Locate every uninfected red blood cell.
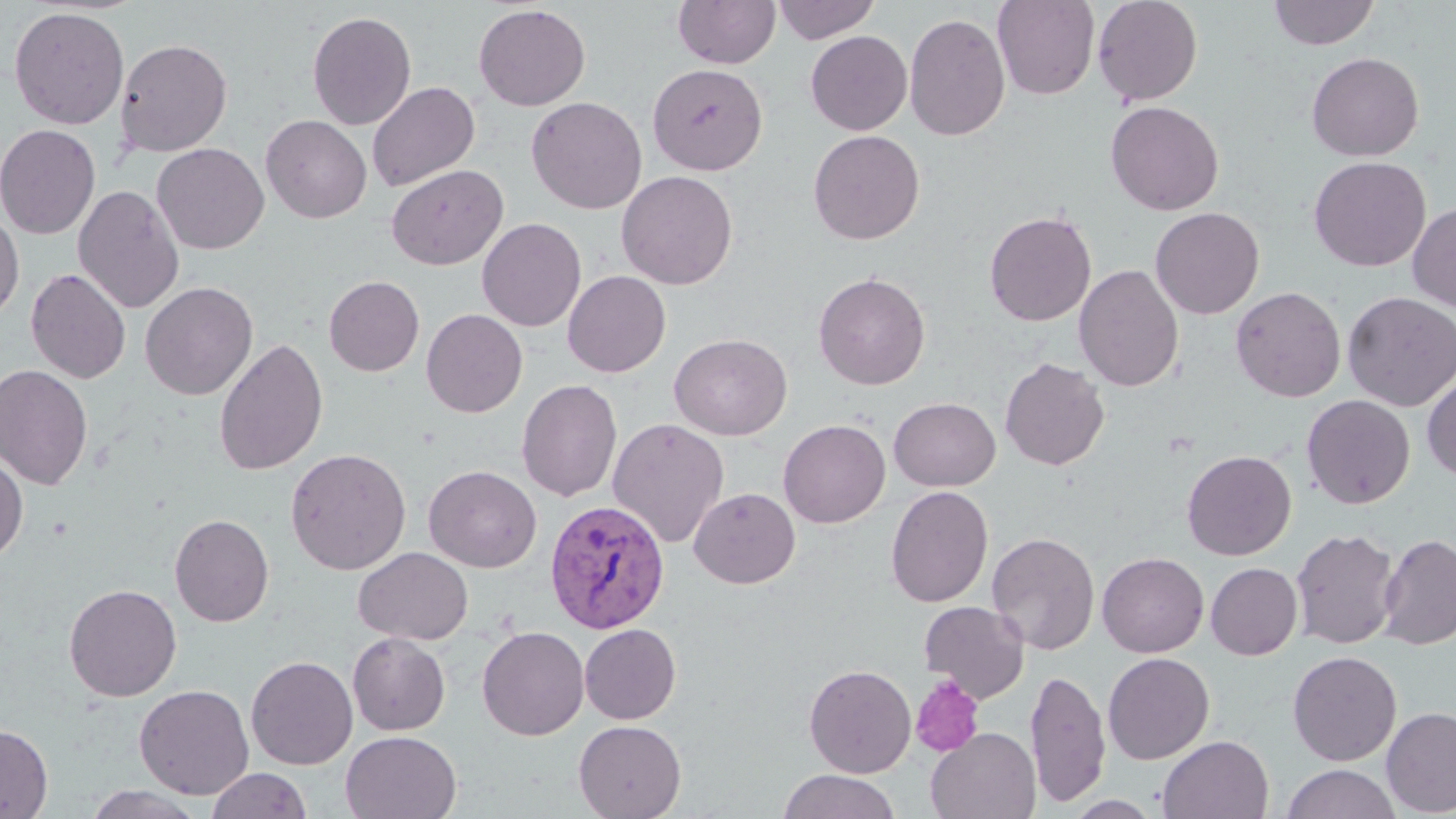
Approximate bounding boxes as named x1/y1/x2/y2 corners in pixels.
Uninfected red blood cells: (x1=673, y1=0, x2=781, y2=69), (x1=772, y1=0, x2=880, y2=44), (x1=992, y1=0, x2=1099, y2=100), (x1=1092, y1=0, x2=1203, y2=106), (x1=1268, y1=0, x2=1380, y2=49), (x1=473, y1=4, x2=591, y2=111), (x1=8, y1=6, x2=129, y2=129), (x1=307, y1=11, x2=416, y2=130), (x1=904, y1=12, x2=1010, y2=141), (x1=805, y1=30, x2=912, y2=135), (x1=115, y1=38, x2=233, y2=157), (x1=1306, y1=52, x2=1425, y2=161), (x1=647, y1=63, x2=768, y2=175), (x1=368, y1=81, x2=480, y2=192), (x1=526, y1=97, x2=647, y2=214), (x1=1105, y1=100, x2=1224, y2=216), (x1=261, y1=115, x2=372, y2=223), (x1=0, y1=124, x2=101, y2=239), (x1=808, y1=130, x2=925, y2=244), (x1=152, y1=143, x2=269, y2=254), (x1=1308, y1=156, x2=1431, y2=272), (x1=386, y1=164, x2=509, y2=269), (x1=616, y1=170, x2=738, y2=290), (x1=73, y1=184, x2=185, y2=314), (x1=1408, y1=202, x2=1456, y2=311), (x1=1150, y1=207, x2=1265, y2=319), (x1=984, y1=210, x2=1097, y2=326), (x1=0, y1=211, x2=24, y2=322), (x1=477, y1=218, x2=586, y2=332), (x1=1074, y1=264, x2=1184, y2=392), (x1=25, y1=268, x2=131, y2=383), (x1=563, y1=270, x2=671, y2=377), (x1=813, y1=272, x2=931, y2=390), (x1=323, y1=275, x2=424, y2=376), (x1=140, y1=281, x2=258, y2=400), (x1=1230, y1=286, x2=1346, y2=402), (x1=1342, y1=291, x2=1456, y2=411), (x1=421, y1=309, x2=528, y2=417), (x1=669, y1=333, x2=792, y2=440), (x1=213, y1=337, x2=329, y2=476), (x1=999, y1=358, x2=1110, y2=471), (x1=0, y1=364, x2=94, y2=490), (x1=1422, y1=371, x2=1456, y2=482), (x1=516, y1=379, x2=622, y2=502), (x1=1302, y1=394, x2=1415, y2=509), (x1=889, y1=397, x2=1000, y2=491), (x1=607, y1=418, x2=729, y2=548), (x1=778, y1=418, x2=890, y2=528), (x1=285, y1=447, x2=412, y2=575), (x1=1182, y1=449, x2=1297, y2=560), (x1=0, y1=451, x2=28, y2=562), (x1=424, y1=465, x2=541, y2=572), (x1=885, y1=485, x2=993, y2=607), (x1=689, y1=487, x2=800, y2=588), (x1=169, y1=513, x2=274, y2=627), (x1=1290, y1=528, x2=1400, y2=649), (x1=986, y1=532, x2=1100, y2=654), (x1=1378, y1=533, x2=1456, y2=649), (x1=353, y1=547, x2=473, y2=645), (x1=1097, y1=552, x2=1209, y2=657), (x1=1206, y1=563, x2=1302, y2=660), (x1=63, y1=583, x2=182, y2=702), (x1=919, y1=600, x2=1030, y2=703), (x1=579, y1=624, x2=681, y2=724), (x1=477, y1=626, x2=589, y2=740), (x1=347, y1=632, x2=451, y2=735), (x1=1287, y1=650, x2=1402, y2=766), (x1=1102, y1=652, x2=1214, y2=764), (x1=246, y1=655, x2=358, y2=770), (x1=804, y1=663, x2=916, y2=778), (x1=1026, y1=667, x2=1111, y2=807), (x1=134, y1=683, x2=255, y2=800), (x1=1381, y1=707, x2=1456, y2=817), (x1=573, y1=720, x2=686, y2=819), (x1=0, y1=723, x2=53, y2=818), (x1=927, y1=727, x2=1041, y2=819), (x1=341, y1=730, x2=462, y2=819), (x1=1157, y1=734, x2=1274, y2=819), (x1=1282, y1=764, x2=1402, y2=819), (x1=206, y1=768, x2=312, y2=819), (x1=778, y1=769, x2=901, y2=819), (x1=82, y1=785, x2=207, y2=819), (x1=1063, y1=795, x2=1163, y2=818).

slide-level diagnosis = Plasmodium vivax
stain = May-Grünwald-Giemsa
image size = 1456×819 pixels
modality = optical microscopy
platelet locations = approximate bounding boxes as named x1/y1/x2/y2 corners in pixels: (x1=910, y1=674, x2=985, y2=756)
Plasmodium vivax-infected red blood cell locations = approximate bounding boxes as named x1/y1/x2/y2 corners in pixels: (x1=544, y1=499, x2=670, y2=634)
magnification = 1000x
preparation = thin blood smear
field of view = single